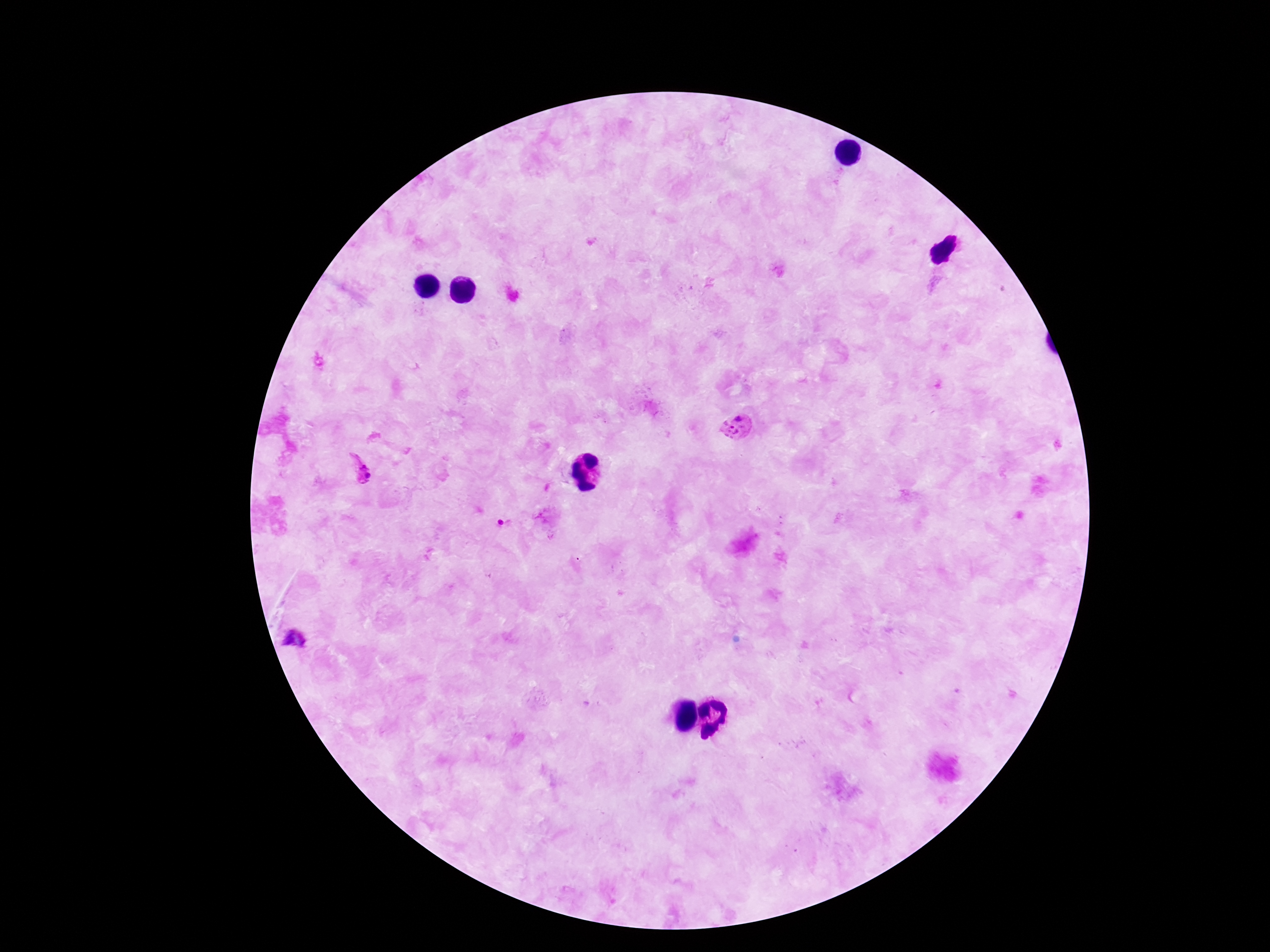
Approximate object centers, in pixels from the top-left corner. Plasmodium parasite locations: (x=738, y=415), (x=729, y=432), (x=361, y=467), (x=501, y=521), (x=293, y=639). Image is 1270×952 pixels. 100x magnification. Thick peripheral-blood smear. Patient malaria status: infected. Single field of view. Smartphone photograph taken through the microscope eyepiece. Giemsa stain.